Locate every leukocyte (white blood cell).
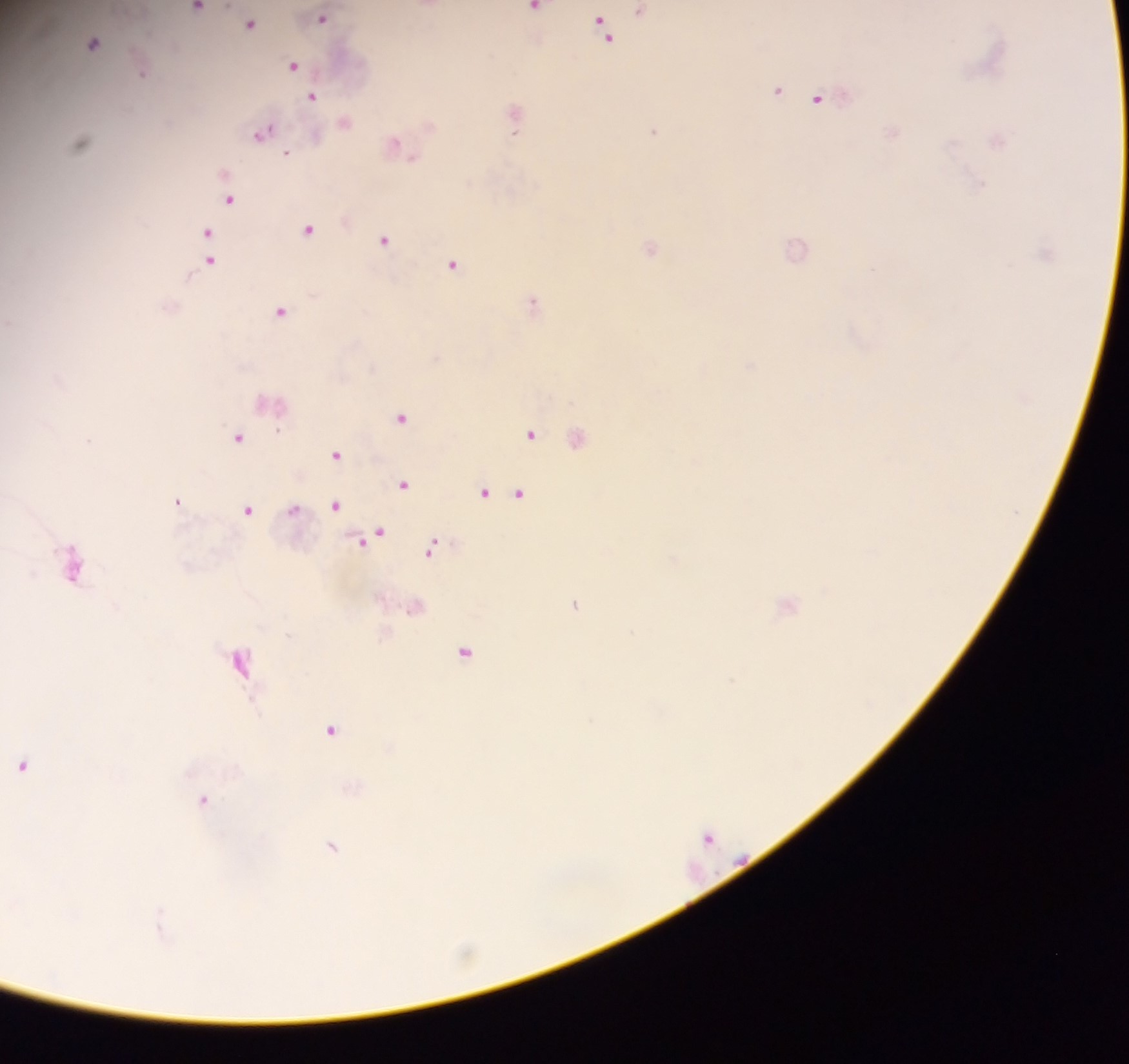

Approximate centers as (x, y) in pixels.
Leukocytes: (574, 436).

Summary:
  - Malaria parasite locations: (198, 8), (535, 8), (641, 10), (322, 18), (251, 22), (604, 26), (93, 43), (294, 65), (143, 72), (777, 90), (313, 96), (818, 98), (515, 118), (654, 130), (264, 132), (81, 142), (395, 145), (288, 153), (230, 198), (309, 229), (208, 234), (384, 240), (651, 247), (796, 249), (210, 257), (454, 264), (534, 304), (281, 310), (402, 417), (532, 434), (238, 437), (337, 454), (403, 483), (485, 492), (520, 493), (178, 501), (335, 504), (294, 508), (248, 509), (375, 536), (432, 547), (73, 564), (575, 603), (788, 603), (465, 651), (240, 660), (732, 681), (331, 729), (23, 765), (204, 799), (708, 836), (332, 845), (161, 924)
  - Image size: 1129×1064 pixels
  - Field of view: single
  - Preparation: thick blood film
  - Country: Ghana
  - Capture: mobile-phone photograph through a microscope